Locate and identify every blood parasite.
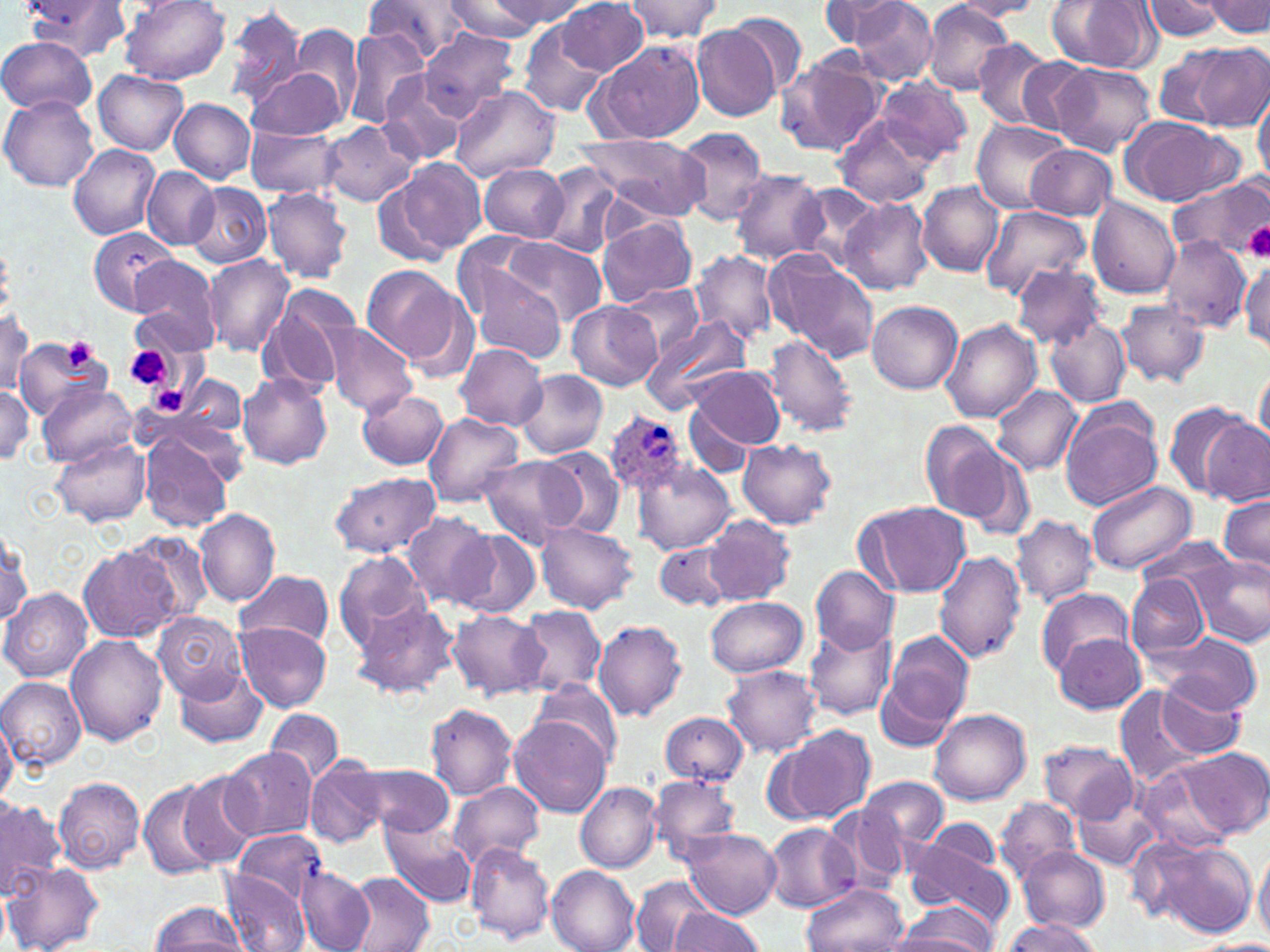

Approximate bounding boxes as [x1, y1, x2, y2] in pixels.
Plasmodium ovale-infected red blood cells: [605, 409, 693, 500].
No Plasmodium falciparum, Plasmodium malariae, Plasmodium vivax, Babesia divergens, or Trypanosoma brucei observed.

slide-level diagnosis = Plasmodium ovale
image size = 1270×952 pixels
magnification = 1000x
uninfected red blood cell locations = approximate bounding boxes as [x1, y1, x2, y2] in pixels: [21, 0, 127, 61], [443, 0, 549, 40], [490, 0, 583, 30], [621, 0, 723, 41], [1046, 0, 1158, 72], [1143, 0, 1226, 43], [1206, 0, 1270, 36], [120, 1, 231, 85], [362, 1, 468, 65], [555, 1, 649, 75], [817, 1, 905, 45], [848, 1, 939, 85], [951, 1, 1046, 20], [921, 2, 1015, 94], [222, 3, 311, 109], [726, 10, 809, 99], [518, 18, 611, 119], [690, 23, 784, 121], [291, 27, 363, 118], [417, 28, 517, 119], [341, 30, 428, 129], [0, 37, 97, 115], [587, 38, 706, 144], [974, 40, 1060, 132], [1184, 40, 1270, 132], [1152, 46, 1241, 128], [774, 52, 886, 157], [1012, 55, 1096, 136], [1048, 62, 1155, 155], [247, 65, 349, 141], [93, 70, 188, 154], [377, 70, 466, 166], [876, 77, 972, 164], [448, 84, 560, 182], [1253, 89, 1269, 184], [0, 95, 99, 193], [168, 97, 254, 184], [833, 115, 936, 208], [971, 120, 1070, 214], [1119, 120, 1243, 207], [318, 121, 417, 208], [246, 126, 341, 197], [674, 128, 769, 225], [575, 132, 710, 222], [1026, 144, 1117, 221], [68, 145, 160, 240], [385, 157, 484, 260], [539, 163, 632, 259], [478, 164, 569, 242], [142, 167, 219, 249], [729, 169, 829, 263], [1170, 175, 1270, 260], [917, 181, 1005, 276], [187, 182, 272, 268], [792, 183, 886, 270], [263, 186, 352, 283], [1087, 196, 1182, 299], [838, 197, 933, 294], [982, 206, 1092, 303], [596, 217, 697, 305], [89, 228, 181, 316], [453, 233, 548, 318], [502, 236, 605, 325], [1159, 236, 1251, 334], [692, 249, 779, 343], [761, 249, 880, 365], [202, 254, 293, 356], [1241, 257, 1270, 354], [126, 258, 222, 353], [361, 263, 461, 364], [1011, 263, 1107, 346], [470, 266, 566, 363], [258, 284, 361, 398], [623, 284, 707, 358], [566, 301, 661, 391], [867, 301, 962, 393], [1114, 301, 1210, 387], [1, 311, 34, 393], [1045, 315, 1130, 408], [639, 317, 751, 414], [942, 319, 1042, 423], [326, 326, 414, 416], [765, 335, 859, 438], [17, 340, 98, 419], [456, 343, 548, 430], [1253, 364, 1269, 448], [685, 366, 786, 454], [515, 370, 608, 460], [237, 373, 333, 470], [180, 374, 246, 438], [37, 383, 136, 467], [993, 385, 1082, 476], [0, 387, 35, 462], [358, 388, 450, 470], [1166, 403, 1254, 499], [683, 405, 759, 479], [1061, 405, 1163, 511], [423, 412, 525, 507], [1201, 417, 1269, 506], [919, 419, 1015, 525], [141, 433, 233, 533], [739, 438, 838, 530], [951, 439, 1036, 543], [54, 442, 150, 526], [538, 446, 625, 537], [480, 454, 582, 550], [633, 462, 734, 555], [328, 472, 442, 560], [1087, 479, 1195, 576], [1218, 494, 1270, 576], [855, 501, 972, 597], [195, 509, 280, 606], [404, 510, 498, 610], [704, 515, 794, 605], [1011, 515, 1099, 609], [536, 523, 639, 614], [0, 529, 30, 630], [456, 530, 540, 619], [1133, 536, 1239, 601], [655, 541, 733, 612], [79, 546, 179, 640], [932, 550, 1027, 665], [333, 551, 430, 651], [1191, 557, 1270, 648], [810, 565, 899, 654], [233, 569, 335, 649], [1125, 573, 1208, 660], [1037, 587, 1133, 674], [2, 589, 91, 683], [350, 596, 459, 699], [705, 596, 808, 677], [514, 606, 607, 697], [448, 609, 548, 700], [154, 611, 247, 700], [592, 619, 689, 723], [236, 622, 331, 710], [803, 624, 897, 720], [880, 630, 975, 738], [1153, 630, 1262, 717], [65, 634, 167, 746], [1055, 634, 1146, 713], [723, 666, 822, 756], [176, 667, 268, 750], [0, 676, 86, 768], [531, 677, 622, 766], [1151, 681, 1245, 757], [1116, 685, 1216, 788], [426, 703, 517, 799], [266, 709, 343, 784], [929, 709, 1031, 805], [658, 710, 749, 788], [0, 711, 17, 803], [510, 715, 612, 818], [775, 723, 875, 825], [1039, 739, 1139, 822], [221, 748, 318, 842], [1178, 748, 1270, 839], [305, 757, 388, 849], [1136, 759, 1247, 856], [357, 764, 457, 838], [633, 773, 731, 930], [648, 773, 740, 860], [174, 774, 259, 871], [859, 774, 948, 855], [54, 778, 146, 873], [137, 779, 225, 880], [447, 782, 545, 869], [575, 782, 660, 874], [1072, 790, 1166, 872], [994, 796, 1081, 883], [0, 797, 63, 899], [826, 803, 910, 892], [921, 818, 1002, 879], [378, 819, 476, 907], [762, 822, 858, 911], [681, 828, 781, 919], [233, 830, 328, 905], [1132, 836, 1257, 936], [901, 838, 1015, 930], [465, 843, 556, 943], [1017, 846, 1110, 934], [1253, 848, 1270, 940], [5, 864, 102, 951], [295, 866, 374, 952], [547, 866, 640, 952], [345, 871, 434, 952], [222, 873, 308, 952], [630, 876, 716, 951], [801, 882, 908, 952], [150, 900, 248, 951], [889, 901, 997, 950], [670, 908, 765, 952], [999, 920, 1104, 951]
field of view = single
platelet locations = approximate bounding boxes as [x1, y1, x2, y2] in pixels: [1244, 221, 1270, 261], [60, 337, 97, 373], [124, 345, 173, 392], [149, 385, 189, 417]
stain = May-Grünwald-Giemsa
preparation = thin blood smear
modality = light microscopy